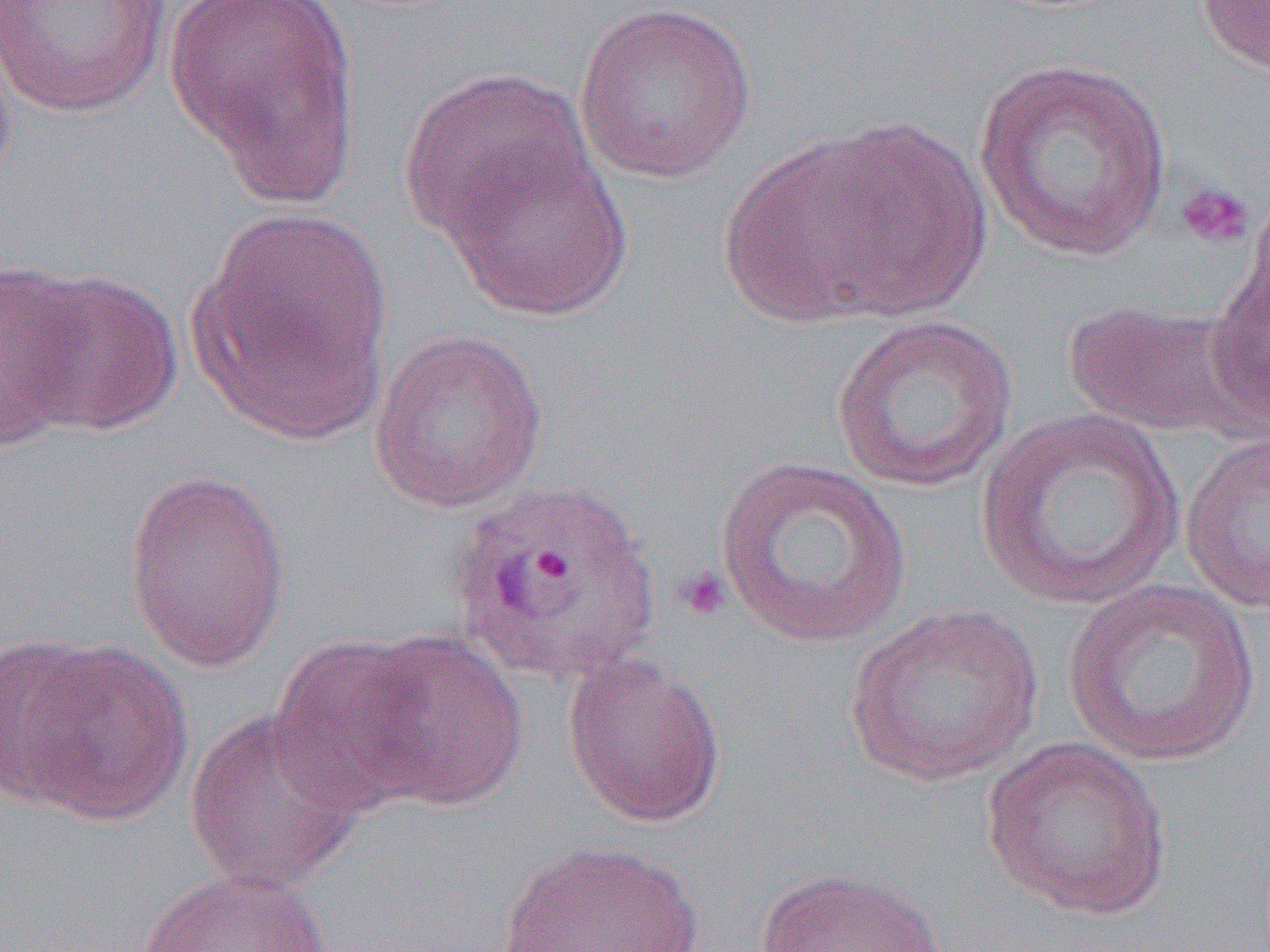
Summary:
  - Coordinate format: approximate bounding boxes as [x1, y1, x2, y2] in pixels
  - Plasmodium ovale-infected red blood cell locations: [446, 476, 661, 689]
  - Platelet locations: [1175, 182, 1256, 250], [676, 566, 732, 622]
  - Uninfected red blood cell locations: [0, 0, 172, 118], [164, 0, 364, 203], [1194, 0, 1270, 75], [573, 1, 758, 186], [0, 23, 20, 201], [973, 57, 1174, 263], [399, 67, 595, 243], [728, 118, 994, 328], [437, 139, 635, 321], [191, 207, 395, 441], [1204, 220, 1269, 438], [0, 259, 91, 448], [5, 266, 183, 438], [1060, 298, 1248, 438], [831, 313, 1019, 493], [369, 328, 548, 514], [975, 407, 1186, 610], [1180, 430, 1270, 614], [714, 454, 913, 648], [122, 467, 292, 672], [1065, 578, 1262, 767], [845, 603, 1043, 788], [352, 629, 530, 812], [267, 634, 440, 815], [0, 636, 104, 807], [11, 639, 194, 827], [561, 652, 727, 828], [184, 708, 364, 893], [980, 736, 1173, 922], [491, 839, 711, 952], [138, 866, 331, 952], [756, 867, 949, 952]
  - Slide-level diagnosis: Plasmodium ovale
  - Magnification: 1000x
  - Preparation: thin blood film
  - Field of view: one of a larger specimen
  - Image size: 1270×952 pixels
  - Modality: optical microscopy